State the blood parasite species.
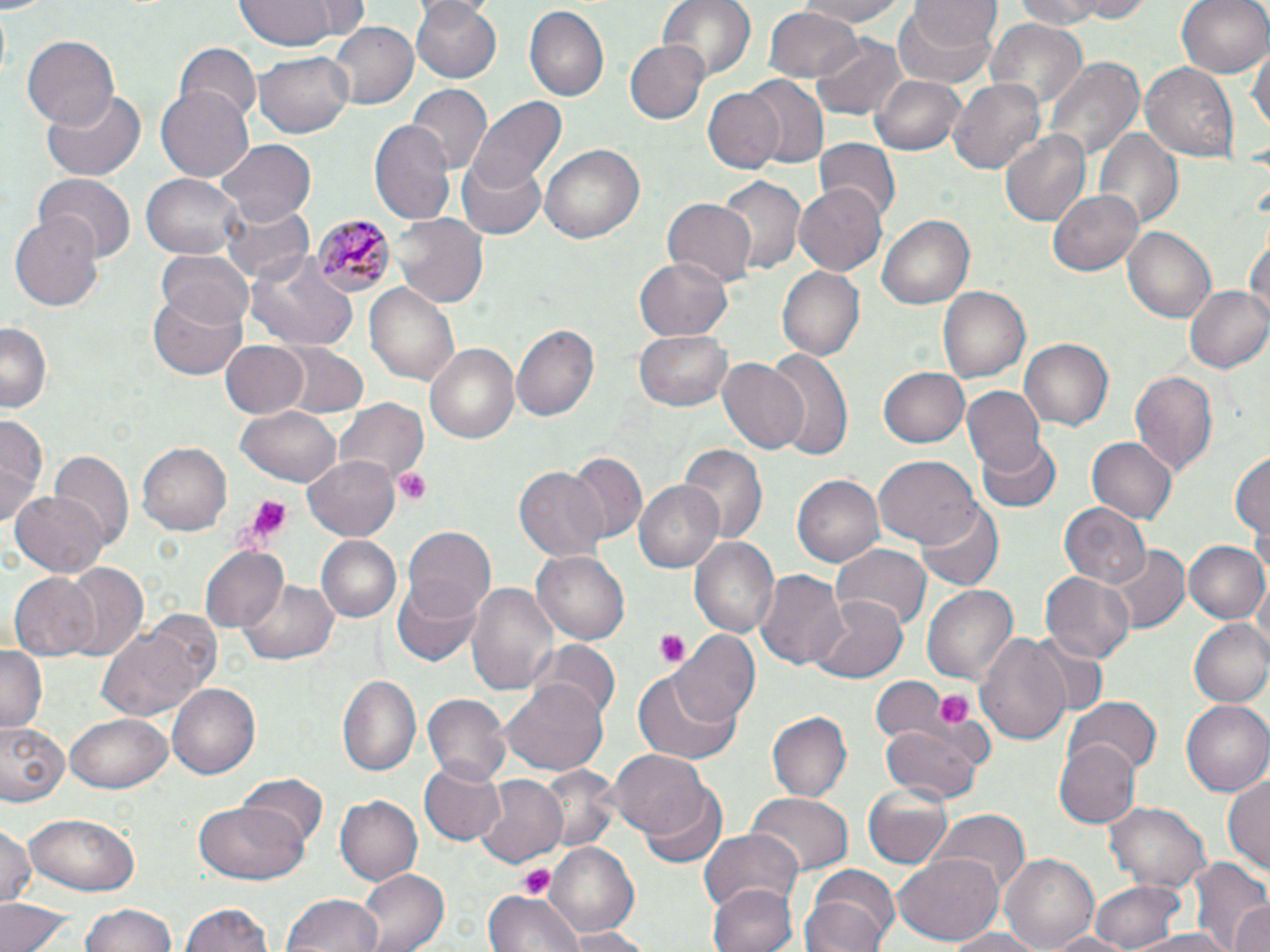

Plasmodium malariae.

Summary:
  - Coordinate format: approximate bounding boxes as (x1, y1, x2, y2) in pixels
  - Platelet locations: (396, 469, 432, 505), (239, 494, 296, 548), (654, 629, 689, 668), (934, 687, 973, 730), (516, 864, 556, 895)
  - Plasmodium malariae-infected red blood cell locations: (312, 212, 394, 297)
  - Uninfected red blood cell locations: (238, 0, 345, 49), (657, 0, 757, 87), (791, 0, 915, 27), (909, 0, 1000, 45), (1004, 0, 1120, 29), (1055, 0, 1160, 21), (1176, 0, 1270, 80), (409, 1, 501, 83), (895, 1, 1002, 88), (524, 5, 607, 103), (763, 7, 865, 84), (984, 18, 1090, 117), (326, 23, 420, 109), (22, 35, 120, 131), (812, 35, 910, 120), (627, 42, 708, 123), (175, 43, 260, 125), (1250, 43, 1268, 139), (255, 52, 355, 137), (1045, 58, 1142, 163), (1140, 63, 1239, 161), (870, 75, 967, 155), (742, 76, 829, 168), (949, 78, 1046, 174), (407, 84, 491, 173), (157, 86, 255, 182), (42, 87, 148, 183), (704, 87, 783, 174), (464, 97, 567, 197), (369, 119, 454, 224), (1096, 128, 1181, 228), (999, 131, 1089, 227), (815, 138, 897, 219), (216, 139, 315, 227), (541, 143, 645, 244), (457, 158, 546, 241), (37, 173, 136, 263), (141, 173, 247, 260), (716, 174, 805, 277), (796, 182, 887, 276), (1051, 189, 1146, 276), (218, 196, 314, 285), (662, 198, 757, 289), (393, 214, 488, 308), (9, 215, 103, 310), (878, 215, 975, 309), (1247, 223, 1269, 325), (1122, 226, 1216, 323), (155, 250, 254, 332), (249, 255, 356, 349), (633, 259, 731, 338), (776, 265, 864, 362), (1183, 283, 1270, 375), (365, 285, 460, 386), (148, 287, 250, 380), (938, 288, 1030, 384), (0, 320, 51, 411), (514, 324, 600, 423), (634, 330, 734, 411), (218, 339, 309, 420), (1020, 339, 1113, 430), (423, 342, 520, 446), (276, 344, 369, 419), (762, 349, 853, 463), (717, 358, 810, 454), (878, 366, 969, 448), (1130, 369, 1218, 475), (964, 386, 1047, 473), (335, 397, 429, 486), (235, 406, 343, 488), (0, 415, 48, 528), (975, 435, 1060, 514), (1087, 436, 1178, 527), (137, 442, 231, 535), (678, 442, 766, 545), (1231, 448, 1268, 547), (53, 449, 131, 549), (568, 454, 648, 544), (873, 456, 981, 549), (303, 457, 401, 540), (517, 466, 611, 562), (792, 475, 883, 568), (633, 480, 725, 573), (10, 490, 108, 577), (914, 502, 1003, 591), (1058, 503, 1150, 589), (401, 524, 496, 616), (315, 536, 402, 624), (690, 536, 780, 637), (1184, 540, 1270, 624), (200, 545, 288, 632), (835, 545, 930, 629), (1107, 546, 1189, 631), (532, 550, 628, 643), (59, 563, 149, 664), (755, 567, 849, 668), (1041, 570, 1135, 664), (9, 571, 100, 660), (391, 575, 483, 665), (467, 578, 561, 696), (242, 580, 337, 665), (922, 583, 1018, 685), (807, 593, 910, 683), (1188, 618, 1270, 708), (100, 622, 207, 721), (975, 630, 1073, 750), (669, 632, 761, 727), (1027, 637, 1109, 719), (531, 641, 622, 723), (0, 648, 45, 732), (631, 672, 743, 766), (336, 673, 421, 776), (871, 677, 951, 744), (167, 682, 261, 776), (501, 683, 609, 775), (424, 694, 511, 786), (1067, 698, 1161, 776), (1181, 698, 1270, 797), (67, 710, 173, 791), (768, 712, 852, 802), (2, 721, 69, 805), (881, 724, 984, 803), (1057, 739, 1142, 831), (610, 748, 713, 841), (420, 761, 506, 846), (537, 765, 621, 851), (1224, 772, 1270, 880), (237, 774, 328, 855), (475, 776, 566, 866), (865, 785, 953, 868), (641, 788, 726, 870), (746, 795, 851, 877), (337, 796, 422, 884), (1106, 800, 1211, 892), (192, 803, 311, 885), (932, 809, 1029, 894), (26, 812, 141, 894), (0, 822, 38, 910), (699, 830, 802, 913), (545, 840, 641, 936), (1000, 851, 1100, 952), (892, 852, 1002, 946), (1188, 856, 1270, 952), (356, 867, 449, 952), (800, 871, 900, 952), (1089, 879, 1188, 951), (709, 882, 798, 952), (483, 890, 581, 952), (280, 894, 386, 952), (0, 898, 74, 952), (181, 900, 279, 952), (1230, 900, 1270, 952), (79, 901, 181, 952), (938, 927, 1051, 951), (556, 928, 663, 950), (1042, 931, 1140, 952), (1126, 931, 1240, 952)
  - Magnification: 1000x
  - Image size: 1270×952 pixels
  - Stain: May-Grünwald-Giemsa
  - Field of view: single
  - Preparation: thin blood film
  - Modality: light microscopy